Name the cell type shown.
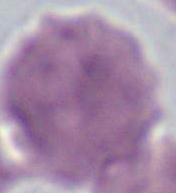
An erythrocyte.

modality: photomicrograph
magnification: 1000x